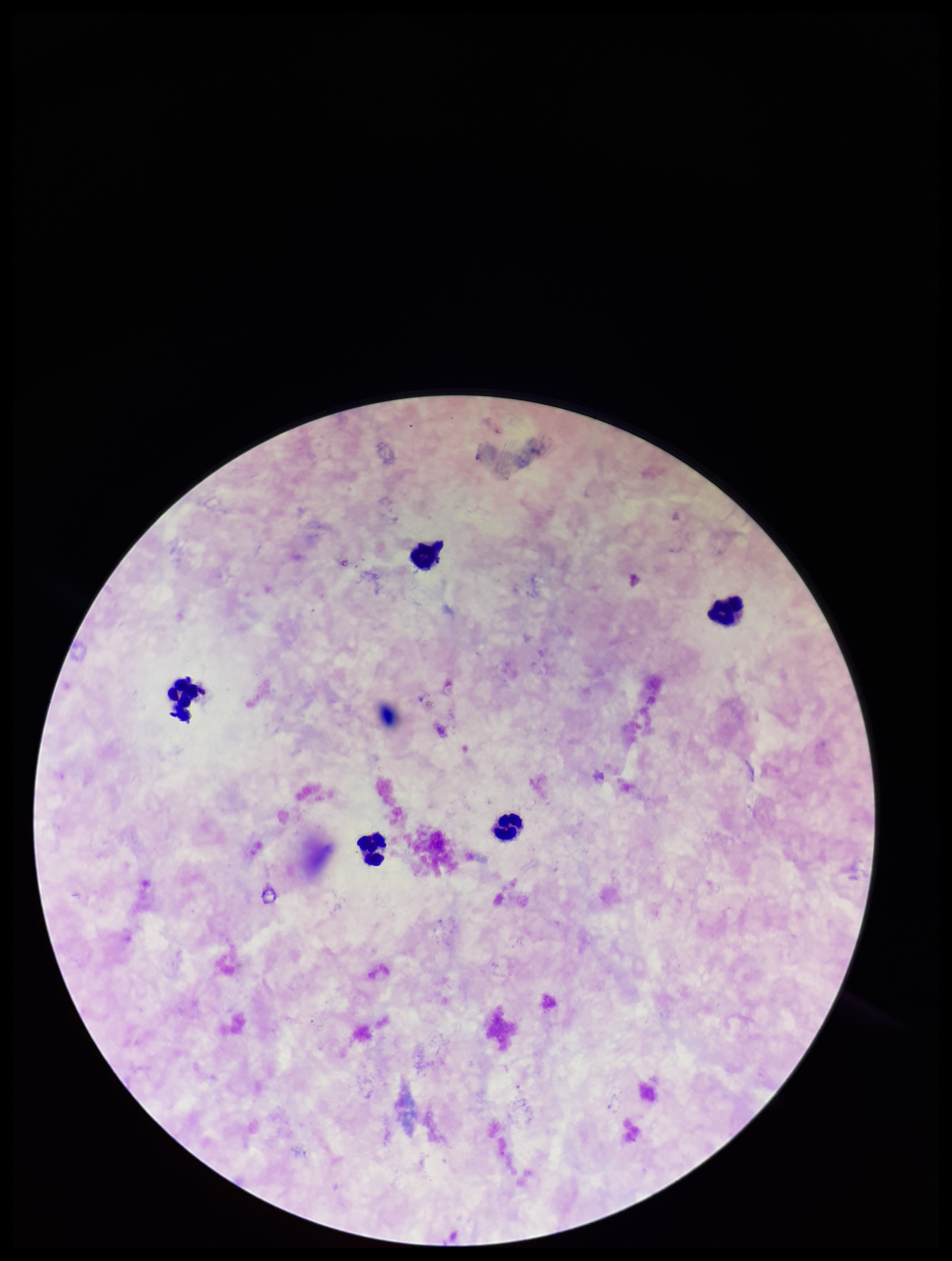
Summary:
  - Capture: smartphone photograph through the microscope eyepiece
  - Field of view: one from this slide
  - Leukocyte count: 5
  - Image size: 952×1261 pixels
  - Plasmodium parasites: none identified
  - Parasite count: 0
  - Patient malaria status: negative
  - Preparation: thick
  - Stain: Giemsa